Identify the parasite.
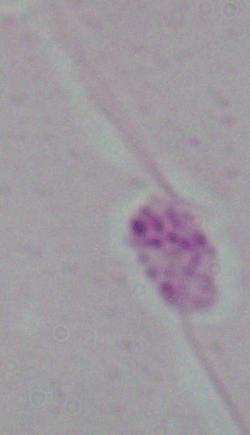

Leishmania.

Photomicrograph. Captured at 1000x magnification.